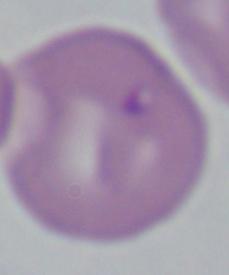
A Babesia parasite is shown. 1000x magnification. Photomicrograph.